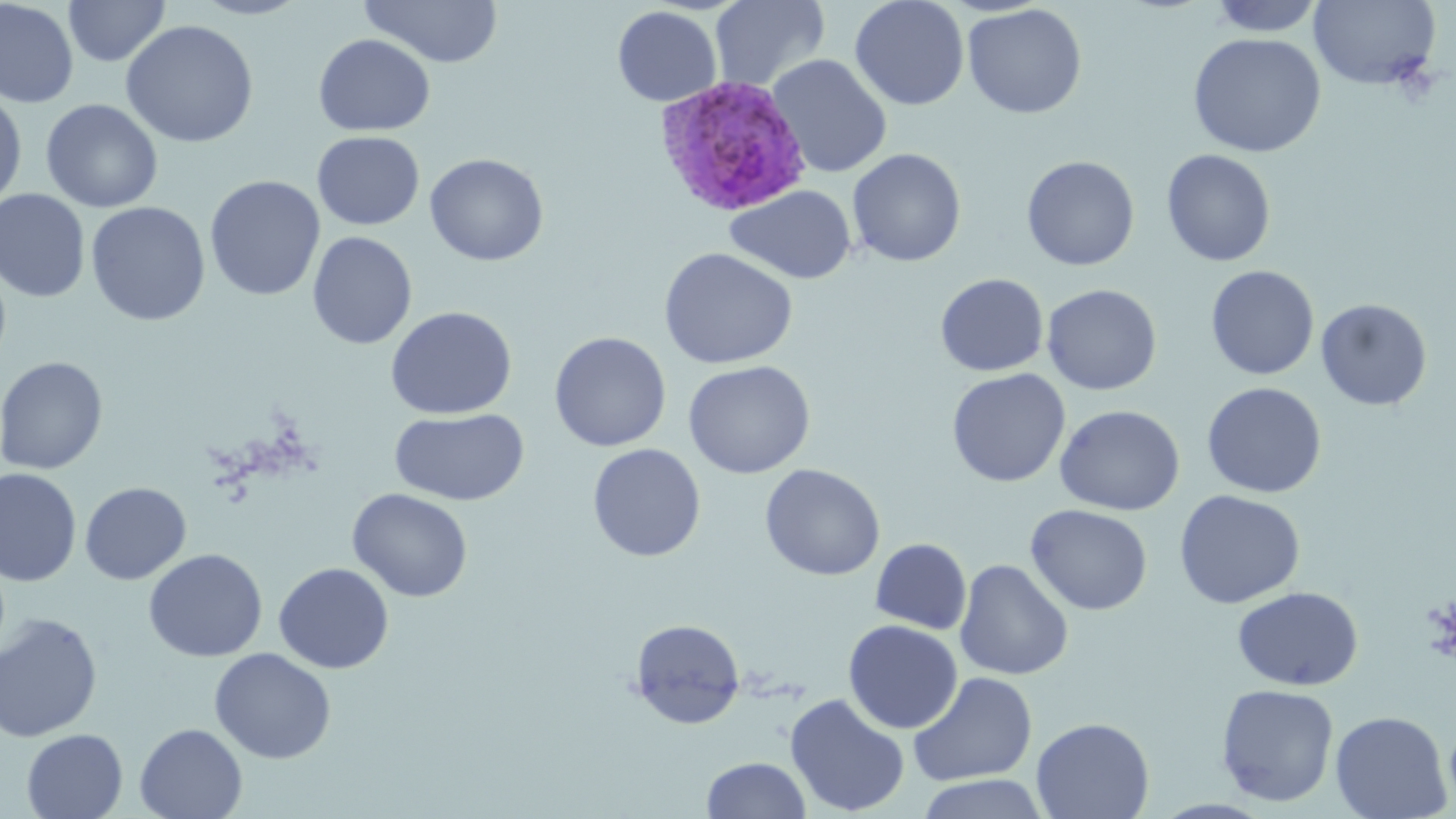
slide-level diagnosis = Plasmodium ovale
modality = optical microscopy
image size = 1456×819 pixels
uninfected red blood cell locations = approximate bounding boxes as (x1,y1)-(x2,y2) corner pairs in pixels: (0,0)-(79,109), (62,0)-(171,67), (189,0)-(312,20), (359,0)-(504,68), (710,0)-(831,91), (849,0)-(969,111), (1206,0)-(1326,36), (1309,0)-(1442,90), (962,3)-(1087,119), (612,6)-(722,107), (120,19)-(259,148), (1187,32)-(1326,158), (313,33)-(435,136), (767,54)-(892,178), (0,88)-(28,211), (41,99)-(163,213), (311,131)-(425,230), (847,148)-(966,267), (1161,149)-(1276,267), (425,153)-(549,266), (1021,155)-(1140,271), (204,175)-(326,302), (725,185)-(857,284), (0,189)-(90,303), (86,201)-(210,326), (307,231)-(417,350), (658,247)-(798,369), (1205,265)-(1319,380), (935,273)-(1049,377), (1041,284)-(1162,395), (1316,298)-(1432,411), (385,306)-(517,419), (549,332)-(671,451), (0,357)-(107,474), (682,360)-(816,479), (946,368)-(1070,487), (1201,381)-(1326,498), (1055,404)-(1184,516), (390,408)-(529,506), (587,443)-(706,562), (759,463)-(885,580), (0,468)-(82,587), (80,482)-(191,585), (347,488)-(473,603), (1174,489)-(1305,608), (1025,504)-(1152,615), (870,538)-(971,634), (143,548)-(267,662), (954,559)-(1074,681), (273,562)-(394,674), (1232,586)-(1363,691), (0,613)-(103,743), (628,618)-(745,729), (843,620)-(963,733), (209,648)-(336,764), (908,671)-(1038,786), (1216,684)-(1340,807), (785,693)-(910,817), (1329,710)-(1452,819), (1031,717)-(1155,819), (135,723)-(247,819), (21,728)-(128,819), (701,756)-(811,818), (914,773)-(1050,819)
Plasmodium ovale-infected red blood cell locations = approximate bounding boxes as (x1,y1)-(x2,y2) corner pairs in pixels: (654,75)-(812,218)
field of view = one of a larger specimen
stain = May-Grünwald-Giemsa
preparation = thin blood film
magnification = 1000x